Identify the blood parasite species.
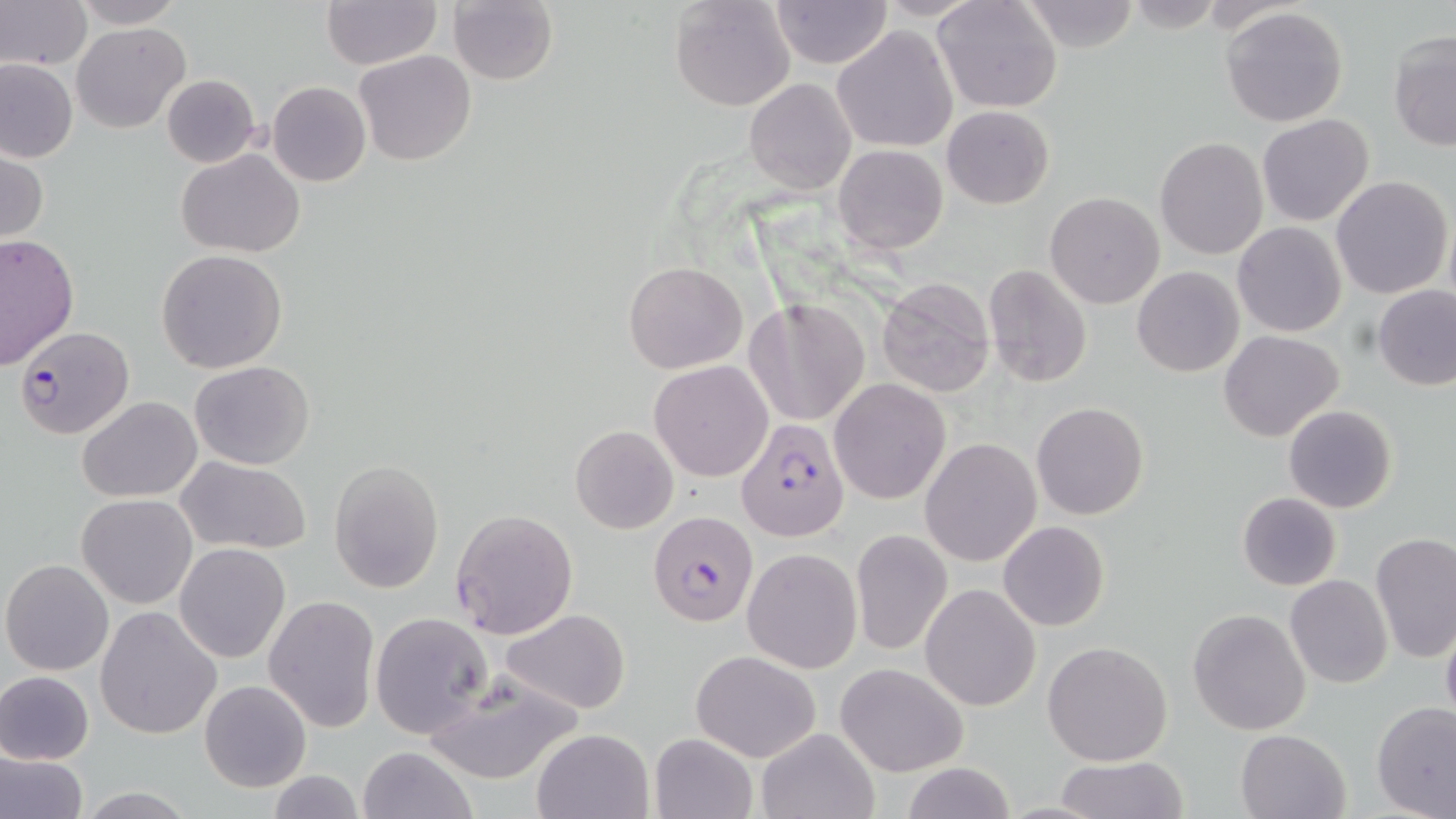
Plasmodium falciparum.

Summary:
  - Coordinate format: approximate bounding boxes as (x1,y1)-(x2,y2) corner pairs in pixels
  - Plasmodium falciparum-infected red blood cell locations: (14,326)-(130,437), (735,416)-(850,542), (650,509)-(758,628)
  - Uninfected red blood cell locations: (2,0)-(89,71), (320,0)-(440,69), (448,0)-(559,85), (669,0)-(796,112), (767,0)-(892,68), (931,0)-(1062,115), (71,1)-(185,27), (1020,1)-(1142,53), (1219,7)-(1349,128), (72,23)-(190,133), (831,25)-(959,153), (1388,30)-(1455,152), (355,50)-(475,166), (0,58)-(78,162), (162,74)-(262,169), (744,78)-(856,195), (267,81)-(371,187), (942,105)-(1053,208), (1257,114)-(1374,226), (1155,137)-(1268,258), (833,144)-(948,254), (1,147)-(49,246), (175,148)-(304,259), (1331,174)-(1452,299), (1044,192)-(1165,309), (1233,222)-(1347,338), (0,232)-(78,368), (156,249)-(288,373), (623,261)-(748,373), (637,261)-(759,476), (982,265)-(1092,388), (1132,266)-(1244,378), (876,276)-(996,396), (1374,286)-(1456,390), (745,299)-(872,426), (1217,329)-(1343,441), (190,359)-(316,469), (649,360)-(775,482), (828,378)-(951,505), (78,397)-(202,502), (1030,402)-(1149,521), (1283,403)-(1398,513), (569,425)-(678,533), (919,438)-(1042,567), (175,456)-(311,556), (330,459)-(444,594), (1236,491)-(1342,591), (78,494)-(197,608), (450,509)-(579,640), (996,521)-(1109,633), (850,528)-(954,658), (1370,532)-(1456,664), (174,543)-(290,663), (742,548)-(863,674), (1,558)-(115,675), (1285,575)-(1394,690), (920,584)-(1042,713), (263,594)-(379,732), (95,605)-(222,741), (1186,608)-(1311,734), (501,609)-(632,714), (369,611)-(494,741), (1441,621)-(1456,729), (1042,640)-(1173,766), (691,648)-(822,762), (835,662)-(968,776), (419,667)-(582,785), (0,670)-(96,765), (199,679)-(313,792), (1371,702)-(1456,819), (531,727)-(655,819), (756,727)-(879,819), (1236,728)-(1349,819), (650,732)-(759,819), (358,746)-(475,819), (0,748)-(88,819), (1055,756)-(1188,818), (900,762)-(1017,819), (265,772)-(367,818), (72,787)-(202,818)
  - Image size: 1456×819 pixels
  - Preparation: thin blood film
  - Magnification: 1000x
  - Modality: light microscopy
  - Stain: May-Grünwald-Giemsa
  - Field of view: one of a larger specimen